Identify the parasite.
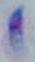
This is Toxoplasma gondii.

Summary:
  - Modality: photomicrograph
  - Magnification: 1000x